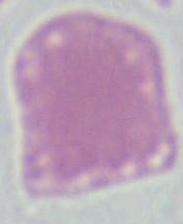
A red blood cell is shown. Captured at 1000x magnification. Micrograph.